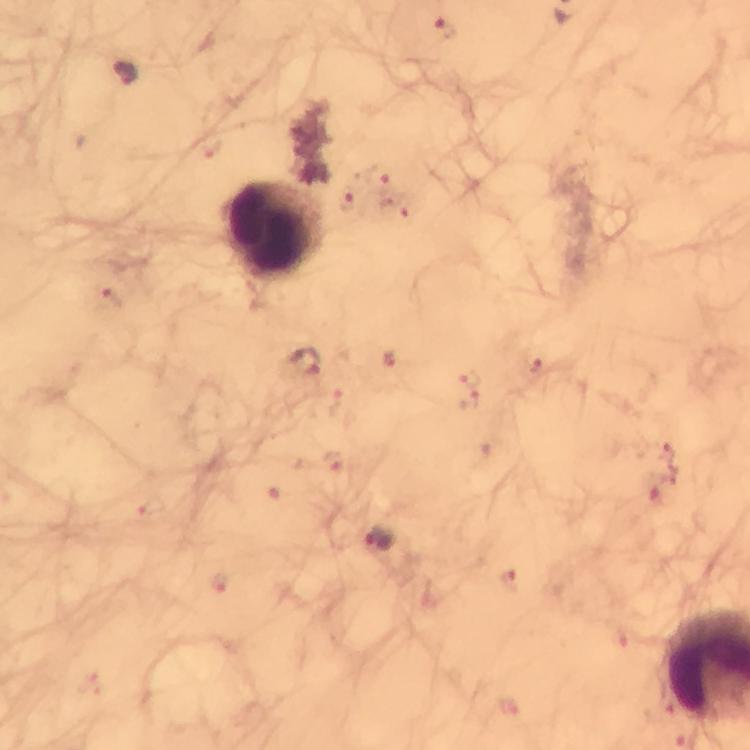

Approximate centers as (x, y) in pixels. Leukocyte locations: (277, 233). Plasmodium parasite locations: (444, 29), (127, 74), (377, 173), (348, 200), (393, 210), (106, 299), (388, 360), (306, 364), (538, 365), (468, 378), (468, 402), (336, 461), (379, 540), (511, 578). Giemsa stain. Thick smear. Image is 750×750 pixels. Smartphone photograph taken through a microscope. From a diagnostic examination for malaria. A crop from one field of view. At 100x magnification. Immersion oil applied.